Classify this cell by malaria status.
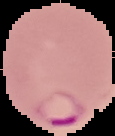
It is parasitized.

preparation = thin blood smear
image size = 115×136 pixels
image type = segmented cell region with the area outside set to black